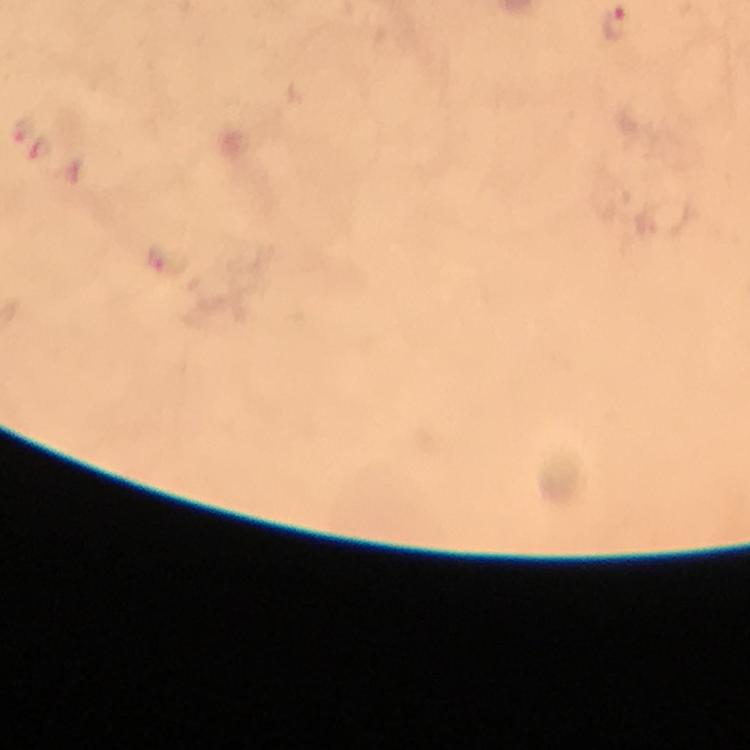

Approximate centers as (x, y) in pixels.
Summary:
  - Malaria parasite locations: (616, 24), (17, 130), (39, 151)
  - Magnification: 100x
  - Preparation: thick blood smear
  - Context: from a malaria diagnostic workup
  - Image size: 750×750 pixels
  - Immersion oil: applied
  - Capture: smartphone photograph through a microscope
  - Stain: Giemsa
  - Cropped from: one field of view